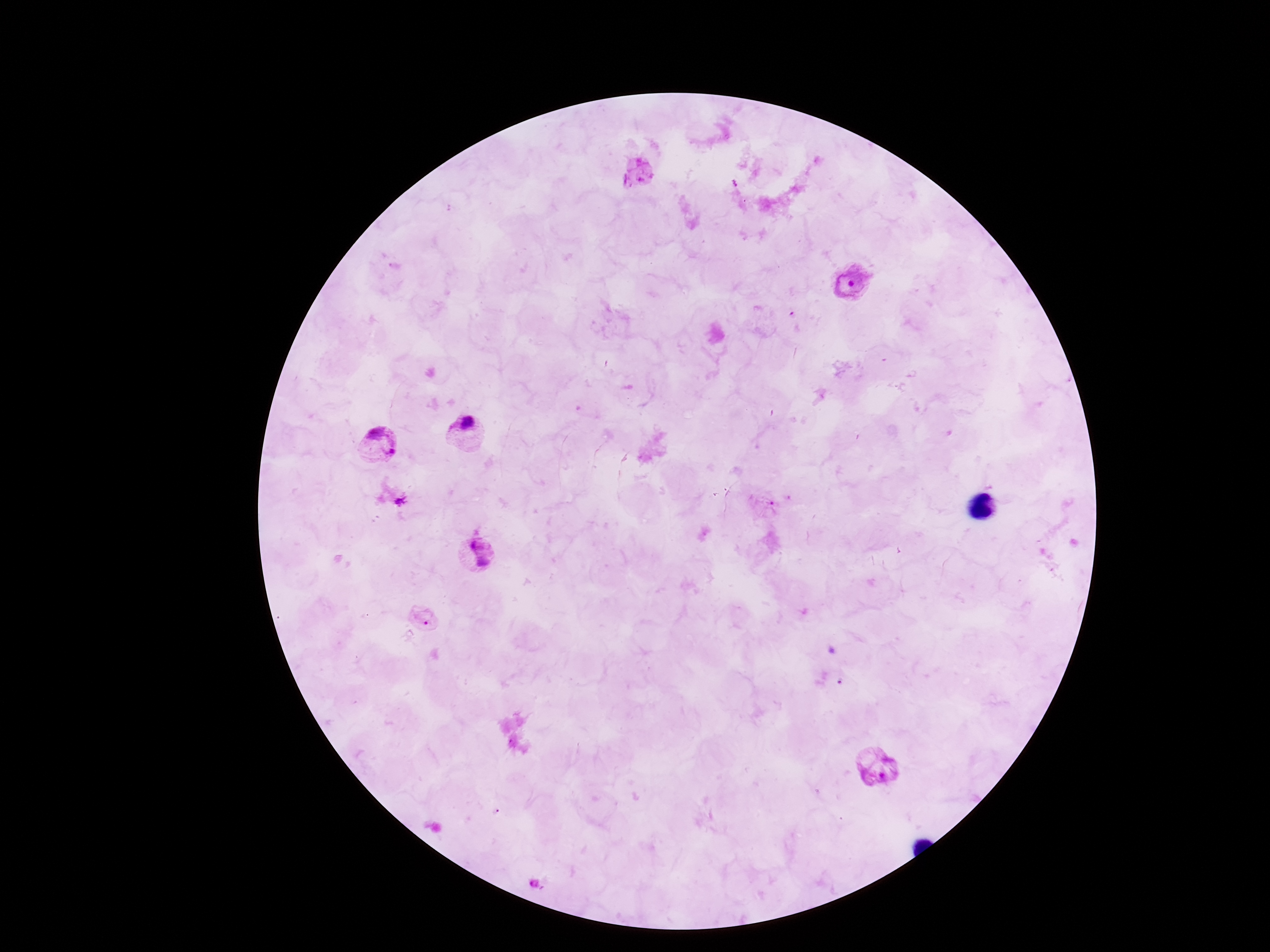
field of view = one from this slide
stain = Giemsa
Plasmodium parasite locations = approximate centers as [x, y] in pixels: [638, 173], [851, 284], [465, 431], [375, 440], [404, 502], [476, 556], [424, 617], [880, 767], [534, 884]
image size = 1270×952 pixels
magnification = 100x
capture = smartphone camera through the microscope eyepiece
patient malaria status = positive
preparation = thick blood smear